State which cell type is depicted.
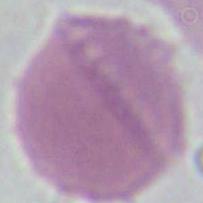
An erythrocyte.

Summary:
  - Magnification: 1000x
  - Modality: micrograph